Locate every Plasmodium parasite and identify its life-cycle stage.
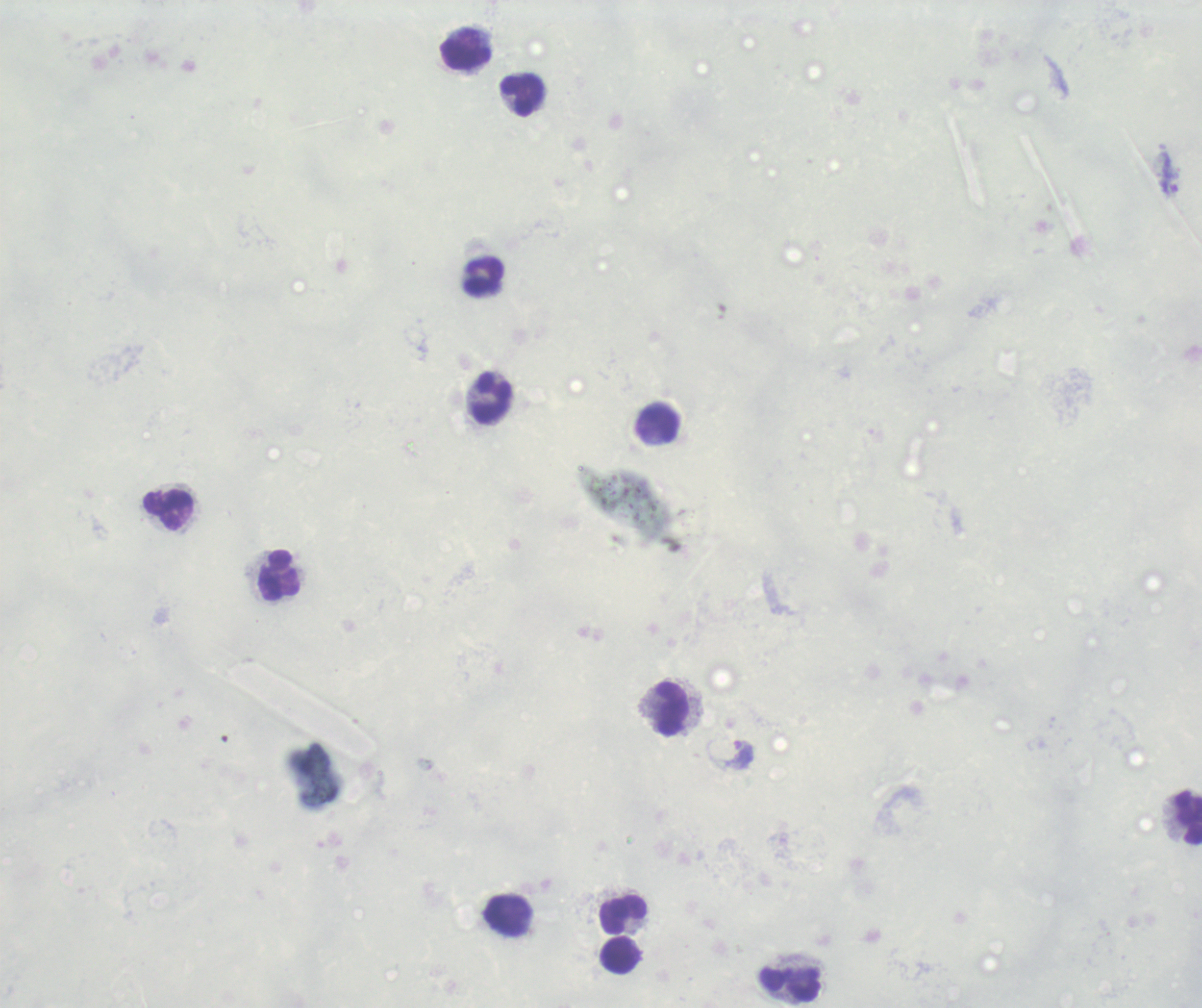

Approximate centers as (x, y) in pixels.
Trophozoites: (1170, 175), (741, 756).
No schizont or gametocyte forms observed.

Approximate centers as (x, y) in pixels.
Summary:
  - Leukocyte locations: (466, 54), (523, 95), (484, 277), (493, 399), (658, 424), (169, 510), (280, 576), (671, 709), (1189, 818), (623, 915), (508, 916), (620, 956), (790, 983)
  - Magnification: 100x
  - Image size: 1202×1008 pixels
  - Stain: Romanowsky
  - Context: previously used in an actual diagnosis
  - Field of view: single
  - Preparation: thick smear of blood
  - Background quality: poor